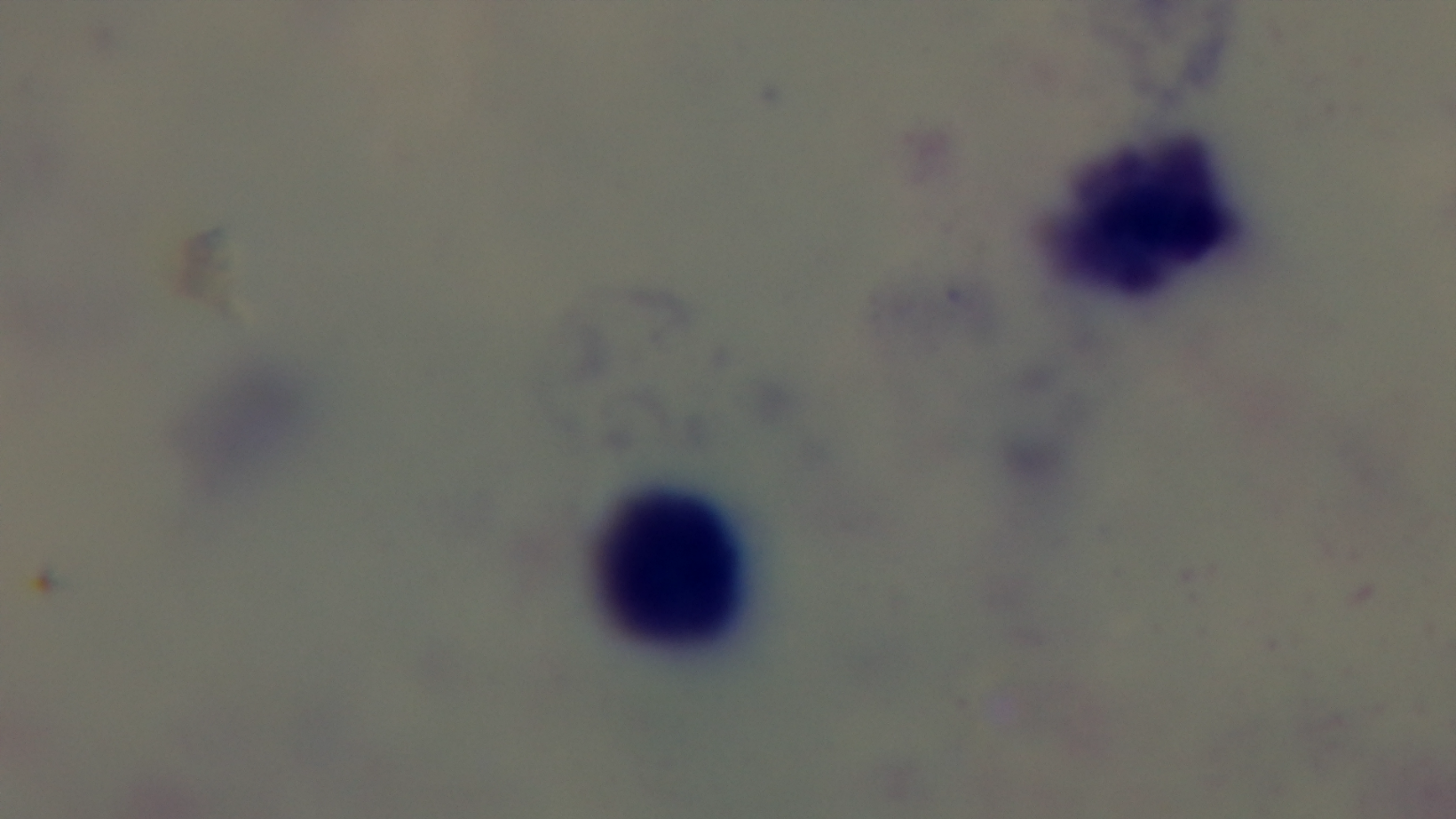 100x oil-immersion objective. Malaria status: uninfected. Giemsa stain. Single field of view. Mounted 4K digital camera. Light microscopy. Preparation: thick smear.